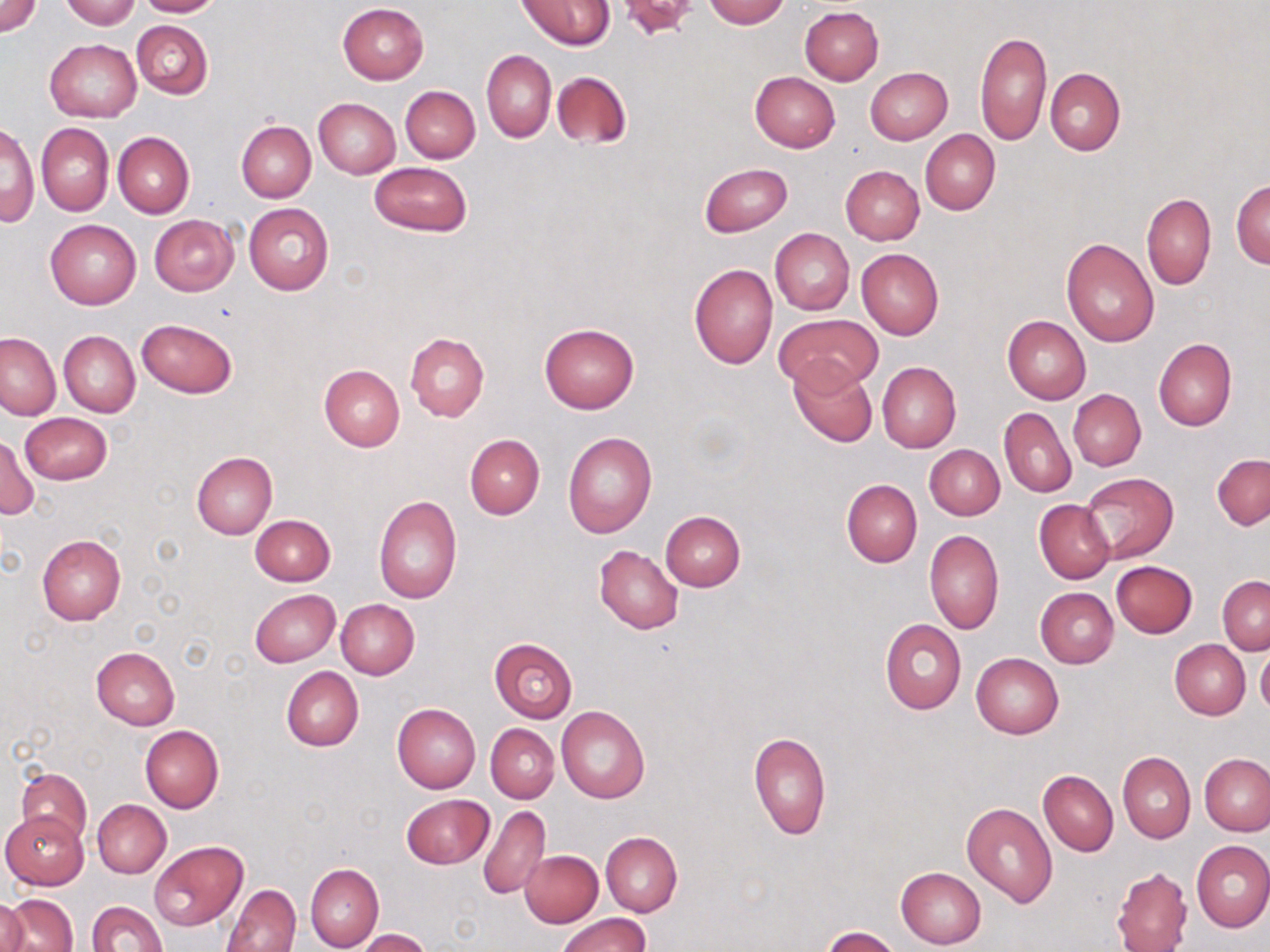

Summary:
  - Coordinate format: approximate bounding boxes as (x1, y1, x2, y2) in pixels
  - Uninfected red blood cell locations: (0, 0, 42, 37), (60, 0, 141, 27), (134, 0, 223, 17), (703, 0, 789, 28), (518, 1, 614, 51), (338, 3, 429, 84), (800, 6, 884, 85), (130, 20, 213, 98), (975, 30, 1052, 147), (45, 39, 140, 122), (481, 50, 557, 142), (865, 67, 952, 145), (1045, 68, 1125, 156), (552, 70, 632, 150), (751, 71, 839, 151), (400, 85, 480, 162), (313, 97, 400, 178), (1, 121, 37, 229), (236, 121, 316, 202), (36, 122, 113, 216), (920, 129, 1000, 215), (113, 132, 194, 218), (369, 162, 471, 236), (700, 163, 792, 237), (840, 165, 924, 245), (1231, 179, 1270, 270), (1142, 193, 1215, 290), (244, 203, 334, 294), (149, 214, 239, 296), (45, 219, 141, 309), (770, 228, 854, 314), (1061, 237, 1158, 347), (857, 248, 944, 340), (688, 264, 778, 369), (777, 313, 883, 391), (1002, 316, 1091, 404), (137, 317, 237, 398), (539, 322, 639, 414), (58, 331, 140, 417), (0, 332, 61, 420), (404, 333, 489, 421), (1153, 338, 1236, 432), (789, 359, 878, 448), (877, 362, 961, 452), (317, 365, 404, 452), (1068, 389, 1145, 471), (999, 406, 1077, 498), (20, 412, 111, 485), (562, 430, 656, 539), (464, 434, 544, 520), (0, 435, 40, 520), (924, 444, 1004, 520), (190, 452, 277, 539), (1212, 454, 1270, 531), (1082, 472, 1178, 564), (841, 478, 922, 568), (373, 494, 462, 604), (1034, 499, 1116, 585), (660, 510, 745, 591), (250, 514, 336, 586), (924, 530, 1003, 635), (37, 534, 127, 626), (594, 545, 683, 635), (1111, 561, 1197, 638), (1218, 576, 1269, 654), (1035, 587, 1118, 668), (249, 590, 340, 667), (336, 599, 419, 679), (880, 619, 967, 714), (488, 636, 579, 722), (1170, 639, 1250, 719), (1257, 645, 1270, 719), (91, 646, 179, 729), (971, 653, 1064, 738), (281, 666, 363, 751), (392, 702, 481, 794), (557, 707, 650, 803), (486, 724, 559, 802), (139, 725, 224, 812), (749, 731, 831, 840), (1117, 751, 1195, 843), (1200, 754, 1269, 834), (17, 768, 91, 847), (1038, 770, 1118, 856), (402, 794, 492, 868), (92, 799, 171, 877), (961, 801, 1058, 907), (478, 805, 550, 901), (1, 811, 88, 889), (600, 830, 682, 917), (1192, 840, 1270, 932), (150, 842, 247, 930), (520, 849, 604, 927), (305, 864, 383, 952), (1111, 865, 1192, 952), (895, 867, 986, 949), (221, 884, 300, 952), (4, 893, 77, 952), (0, 895, 29, 952), (87, 900, 168, 952), (556, 913, 649, 952), (821, 926, 900, 952), (357, 929, 431, 951)
  - Slide-level diagnosis: no evidence of blood parasites
  - Stain: May-Grünwald-Giemsa
  - Magnification: 1000x
  - Preparation: thin blood smear
  - Modality: optical microscopy
  - Image size: 1270×952 pixels
  - Field of view: single